Point out each leukocyte.
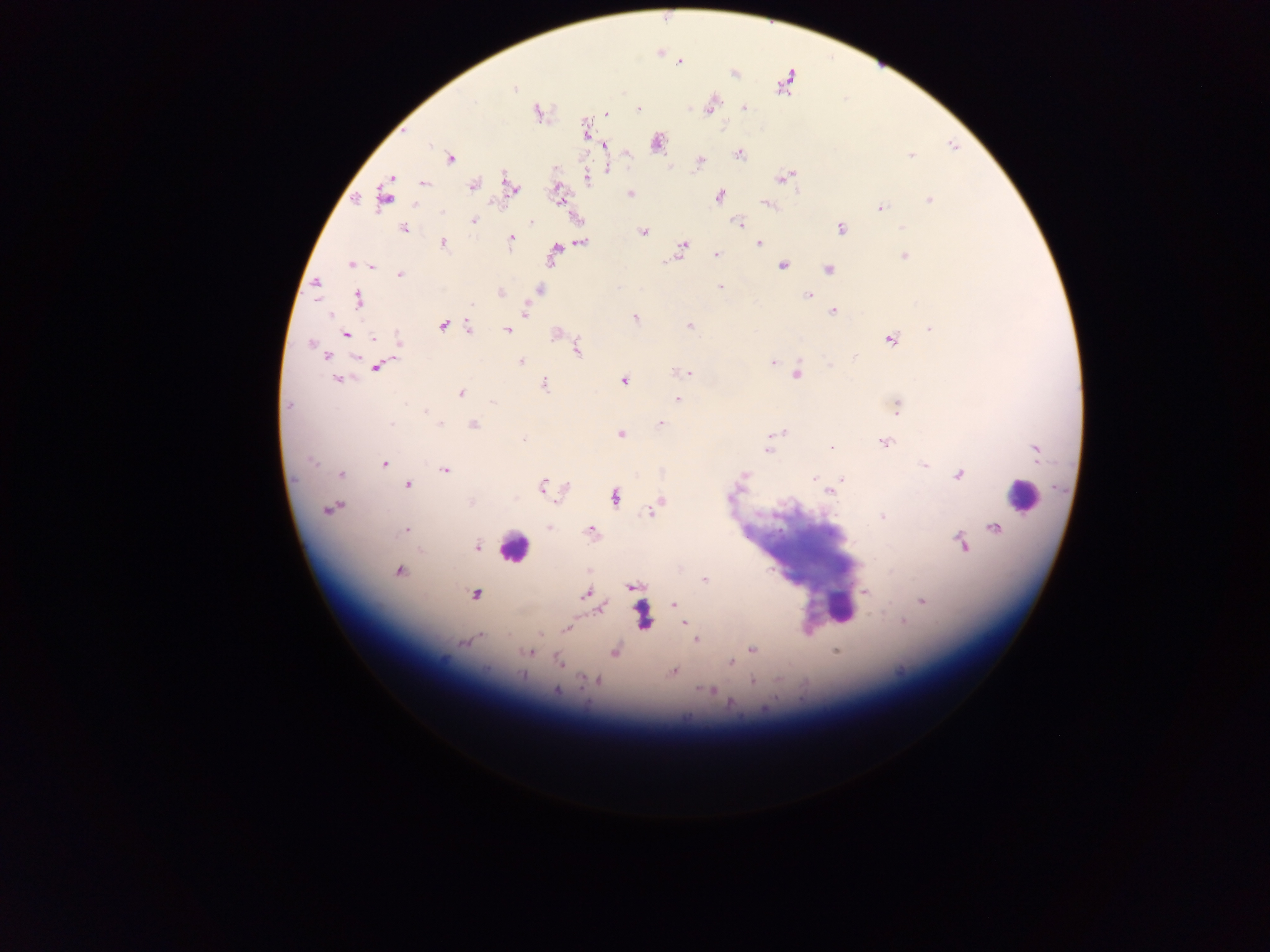
Approximate centers as [x, y] in pixels.
Leukocytes: [1018, 499], [514, 547], [836, 604].

Plasmodium parasite locations: [789, 75], [787, 81], [781, 89], [515, 90], [711, 103], [744, 107], [639, 109], [710, 110], [606, 113], [537, 114], [724, 126], [586, 133], [656, 141], [606, 146], [739, 153], [910, 156], [450, 158], [699, 163], [607, 168], [390, 179], [781, 179], [589, 180], [423, 184], [471, 185], [516, 191], [631, 193], [719, 197], [386, 199], [928, 201], [414, 203], [563, 203], [764, 203], [881, 207], [440, 211], [474, 219], [531, 223], [740, 223], [901, 227], [405, 228], [840, 228], [643, 231], [512, 238], [442, 243], [581, 243], [758, 243], [681, 247], [557, 249], [717, 253], [904, 258], [351, 264], [783, 265], [371, 266], [828, 269], [400, 275], [720, 286], [807, 295], [357, 298], [527, 310], [832, 311], [330, 314], [634, 316], [442, 326], [689, 326], [468, 327], [928, 327], [509, 329], [556, 334], [345, 335], [373, 337], [889, 338], [311, 346], [577, 350], [327, 357], [773, 360], [520, 361], [830, 363], [375, 369], [688, 373], [798, 375], [336, 378], [625, 382], [543, 384], [462, 393], [679, 399], [491, 400], [425, 410], [896, 411], [661, 423], [392, 424], [441, 424], [473, 425], [779, 432], [621, 433], [885, 442], [769, 448], [830, 448], [1036, 453], [312, 460], [386, 465], [924, 465], [444, 470], [341, 473], [958, 474], [746, 477], [814, 479], [844, 480], [568, 483], [407, 484], [544, 486], [830, 490], [615, 498], [663, 501], [659, 505], [332, 507], [656, 509], [327, 510], [882, 517], [549, 526], [590, 528], [406, 529], [994, 529], [956, 535], [962, 542], [477, 547], [399, 571], [703, 581], [630, 588], [863, 592], [474, 594], [584, 595], [924, 600], [674, 605], [600, 610], [642, 618], [901, 622], [686, 623], [567, 628], [695, 640], [463, 642], [753, 648], [522, 652], [836, 652], [558, 660], [732, 663], [674, 672], [524, 676], [598, 679], [752, 681], [583, 683], [557, 691], [712, 691]. Mobile-phone photograph taken through the microscope. Single field of view. Collected in Ghana. Thick blood film. Image is 1270×952 pixels.